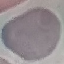

Summary:
  - Result: negative for malaria parasites
  - Stain: Giemsa
  - Preparation: thin blood film
  - Image type: automatically extracted cell patch, resized to 64 × 64 pixels
  - Capture: smartphone through the microscope eyepiece